State which parasite is depicted.
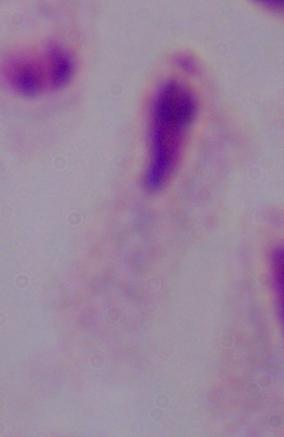
A trichomonad.

1000x magnification. Photomicrograph.